Report the malaria status of this cell.
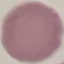
Uninfected.

Thin blood smear. Photographed with a smartphone camera at the microscope eyepiece. Automatically extracted cell patch, resized to 64 × 64 pixels. Giemsa stain.